Classify this cell by malaria status.
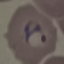
Parasitized.

Cell patch, automatically extracted from a larger field of view and resized to 64 × 64 pixels. Acquired by smartphone through the microscope eyepiece. Giemsa stain. Thin smear of blood.